Comment on the morphology of the erythrocytes.
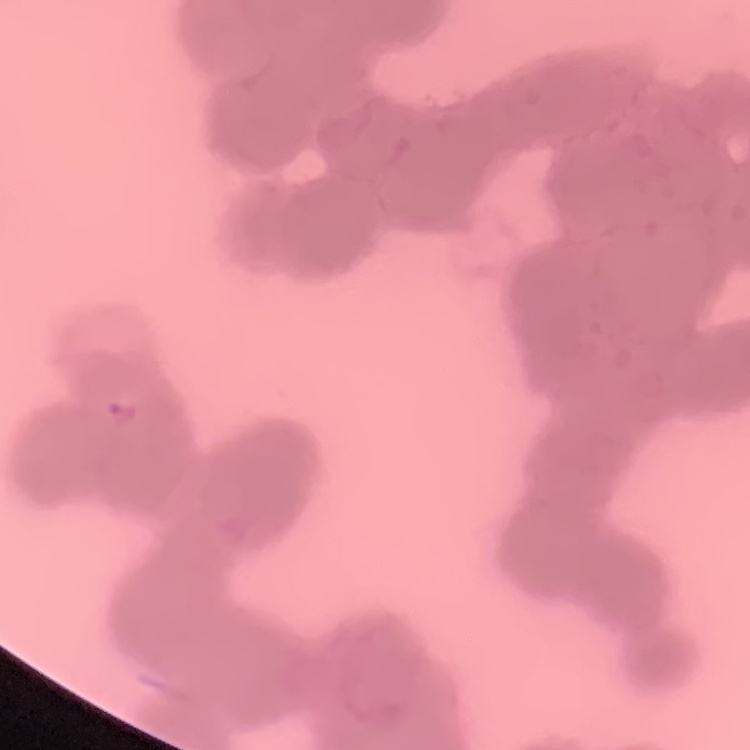
Rouleaux formation.

Summary:
  - Preparation: thin peripheral smear
  - Image type: square crop of a larger photomicrograph
  - Stain: Field's or Giemsa